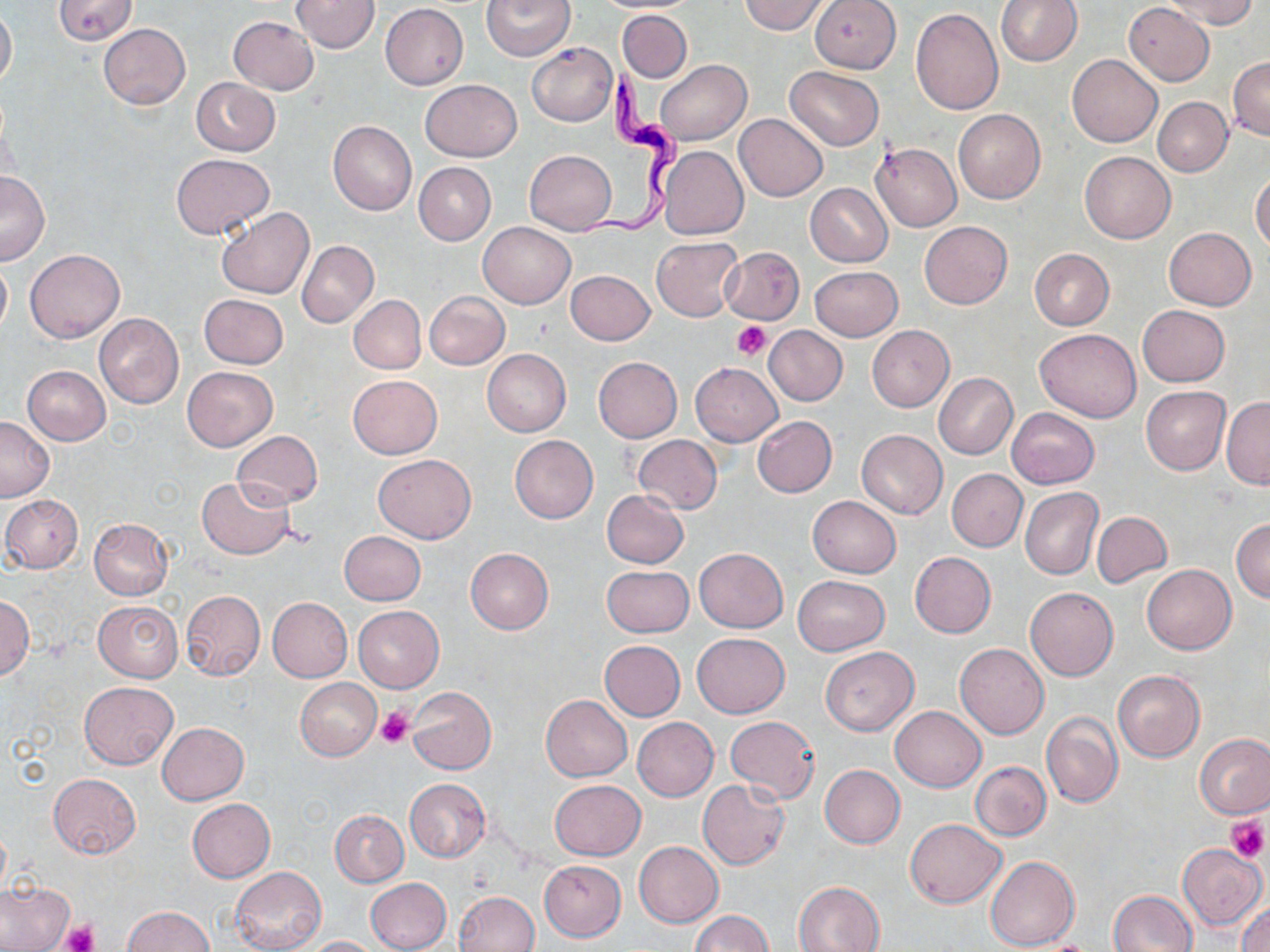

slide-level diagnosis = Trypanosoma brucei
magnification = 1000x
platelet locations = approximate bounding boxes as named x1/y1/x2/y2 corners in pixels: (x1=733, y1=321, x2=771, y2=360), (x1=376, y1=705, x2=414, y2=748), (x1=1227, y1=815, x2=1268, y2=862), (x1=60, y1=920, x2=96, y2=952)
preparation = thin blood film
Trypanosoma brucei locations = approximate bounding boxes as named x1/y1/x2/y2 corners in pixels: (x1=573, y1=61, x2=689, y2=242)
field of view = one of a larger specimen
modality = optical microscopy
uninfected red blood cell locations = approximate bounding boxes as named x1/y1/x2/y2 corners in pixels: (x1=52, y1=0, x2=138, y2=45), (x1=291, y1=0, x2=380, y2=53), (x1=483, y1=0, x2=574, y2=60), (x1=738, y1=0, x2=833, y2=34), (x1=809, y1=0, x2=901, y2=73), (x1=995, y1=0, x2=1083, y2=66), (x1=1163, y1=0, x2=1258, y2=29), (x1=1124, y1=3, x2=1214, y2=85), (x1=0, y1=4, x2=16, y2=90), (x1=381, y1=4, x2=468, y2=89), (x1=911, y1=8, x2=1004, y2=113), (x1=617, y1=10, x2=692, y2=82), (x1=228, y1=16, x2=318, y2=95), (x1=100, y1=24, x2=190, y2=108), (x1=527, y1=42, x2=617, y2=126), (x1=1067, y1=53, x2=1161, y2=147), (x1=1228, y1=56, x2=1269, y2=141), (x1=656, y1=59, x2=750, y2=146), (x1=784, y1=66, x2=884, y2=150), (x1=191, y1=78, x2=280, y2=156), (x1=419, y1=79, x2=521, y2=161), (x1=1153, y1=97, x2=1232, y2=176), (x1=953, y1=110, x2=1045, y2=203), (x1=735, y1=115, x2=827, y2=201), (x1=328, y1=121, x2=417, y2=215), (x1=871, y1=143, x2=962, y2=231), (x1=658, y1=146, x2=748, y2=240), (x1=525, y1=149, x2=617, y2=235), (x1=1080, y1=151, x2=1175, y2=243), (x1=171, y1=152, x2=275, y2=240), (x1=414, y1=162, x2=496, y2=245), (x1=0, y1=170, x2=49, y2=265), (x1=1251, y1=170, x2=1270, y2=251), (x1=806, y1=182, x2=893, y2=267), (x1=216, y1=209, x2=314, y2=298), (x1=478, y1=221, x2=576, y2=308), (x1=919, y1=221, x2=1012, y2=309), (x1=1165, y1=227, x2=1255, y2=310), (x1=651, y1=237, x2=743, y2=322), (x1=297, y1=240, x2=378, y2=326), (x1=719, y1=246, x2=804, y2=323), (x1=26, y1=248, x2=124, y2=342), (x1=1029, y1=248, x2=1115, y2=330), (x1=0, y1=257, x2=11, y2=338), (x1=810, y1=266, x2=902, y2=341), (x1=567, y1=270, x2=654, y2=344), (x1=425, y1=291, x2=510, y2=370), (x1=199, y1=294, x2=288, y2=369), (x1=349, y1=295, x2=425, y2=374), (x1=1137, y1=305, x2=1230, y2=386), (x1=94, y1=313, x2=184, y2=408), (x1=764, y1=325, x2=848, y2=406), (x1=866, y1=325, x2=954, y2=412), (x1=1035, y1=327, x2=1142, y2=422), (x1=483, y1=349, x2=571, y2=436), (x1=593, y1=357, x2=682, y2=442), (x1=691, y1=362, x2=782, y2=445), (x1=23, y1=366, x2=110, y2=445), (x1=182, y1=366, x2=278, y2=451), (x1=933, y1=372, x2=1017, y2=460), (x1=348, y1=374, x2=441, y2=458), (x1=1141, y1=386, x2=1230, y2=474), (x1=1221, y1=397, x2=1269, y2=489), (x1=1006, y1=408, x2=1099, y2=489), (x1=0, y1=416, x2=53, y2=501), (x1=753, y1=416, x2=836, y2=497), (x1=232, y1=430, x2=323, y2=510), (x1=856, y1=430, x2=947, y2=518), (x1=510, y1=435, x2=598, y2=524), (x1=631, y1=435, x2=723, y2=513), (x1=373, y1=453, x2=475, y2=544), (x1=946, y1=469, x2=1027, y2=551), (x1=196, y1=477, x2=295, y2=559), (x1=1020, y1=487, x2=1103, y2=580), (x1=602, y1=490, x2=689, y2=568), (x1=2, y1=496, x2=83, y2=572), (x1=807, y1=496, x2=901, y2=578), (x1=1091, y1=512, x2=1172, y2=588), (x1=90, y1=518, x2=173, y2=599), (x1=1231, y1=518, x2=1270, y2=602), (x1=340, y1=531, x2=427, y2=606), (x1=466, y1=548, x2=553, y2=634), (x1=694, y1=548, x2=788, y2=632), (x1=910, y1=552, x2=996, y2=638), (x1=602, y1=564, x2=693, y2=637), (x1=1141, y1=564, x2=1237, y2=654), (x1=792, y1=575, x2=890, y2=656), (x1=1025, y1=587, x2=1118, y2=681), (x1=180, y1=590, x2=265, y2=680), (x1=0, y1=596, x2=34, y2=678), (x1=268, y1=597, x2=353, y2=681), (x1=93, y1=601, x2=182, y2=681), (x1=354, y1=606, x2=443, y2=692), (x1=692, y1=632, x2=789, y2=717), (x1=599, y1=640, x2=685, y2=721), (x1=955, y1=644, x2=1049, y2=739), (x1=819, y1=646, x2=918, y2=736), (x1=1114, y1=670, x2=1205, y2=762), (x1=295, y1=678, x2=381, y2=760), (x1=80, y1=682, x2=178, y2=769), (x1=407, y1=686, x2=497, y2=775), (x1=541, y1=694, x2=632, y2=781), (x1=890, y1=705, x2=986, y2=791), (x1=1042, y1=713, x2=1123, y2=808), (x1=632, y1=717, x2=718, y2=801), (x1=724, y1=717, x2=820, y2=803), (x1=157, y1=722, x2=249, y2=804), (x1=1196, y1=733, x2=1270, y2=818), (x1=972, y1=761, x2=1051, y2=840), (x1=819, y1=764, x2=905, y2=848), (x1=48, y1=773, x2=142, y2=859), (x1=405, y1=778, x2=490, y2=863), (x1=549, y1=779, x2=646, y2=860), (x1=697, y1=780, x2=790, y2=869), (x1=187, y1=798, x2=275, y2=883), (x1=331, y1=810, x2=408, y2=886), (x1=905, y1=818, x2=1005, y2=908), (x1=633, y1=842, x2=723, y2=927), (x1=1178, y1=844, x2=1266, y2=928), (x1=986, y1=856, x2=1080, y2=950), (x1=539, y1=860, x2=626, y2=941), (x1=231, y1=866, x2=326, y2=952), (x1=365, y1=877, x2=451, y2=952), (x1=0, y1=879, x2=74, y2=951), (x1=793, y1=881, x2=884, y2=952), (x1=1109, y1=890, x2=1197, y2=952), (x1=455, y1=891, x2=540, y2=952), (x1=1235, y1=898, x2=1270, y2=952), (x1=122, y1=906, x2=214, y2=951), (x1=692, y1=911, x2=771, y2=951), (x1=304, y1=936, x2=384, y2=951)
image size = 1270×952 pixels
stain = May-Grünwald-Giemsa